Assess this cell for malaria.
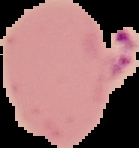
It is parasitized.

Summary:
  - Image type: cell region segmented out of the field of view; surrounding area masked to black
  - Image size: 139×148 pixels
  - Preparation: thin blood smear